Outline each Trypanosoma brucei.
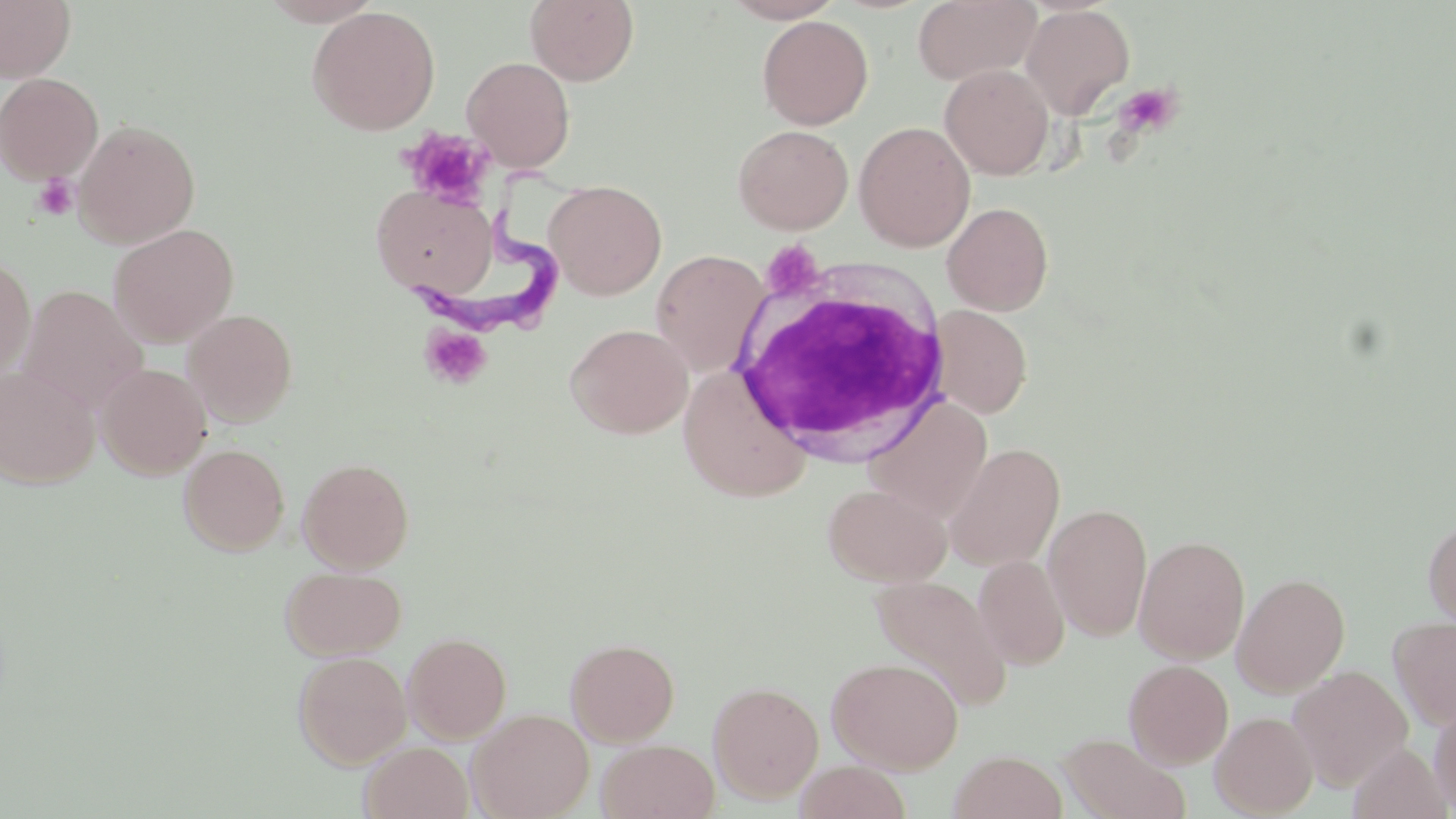
Approximate bounding boxes as (x1, y1, x2, y2) in pixels.
Trypanosoma brucei: (403, 167, 580, 330).

Summary:
  - Platelet locations: (1113, 82, 1183, 139), (401, 129, 494, 209), (32, 173, 80, 221), (760, 240, 825, 302), (419, 323, 492, 390)
  - Uninfected red blood cell locations: (0, 0, 76, 83), (525, 0, 639, 86), (723, 0, 845, 23), (913, 0, 1040, 86), (1020, 4, 1136, 120), (307, 6, 441, 135), (757, 14, 873, 130), (461, 55, 576, 172), (939, 64, 1055, 180), (0, 72, 103, 184), (73, 119, 201, 248), (854, 121, 976, 252), (733, 124, 853, 234), (544, 180, 667, 300), (371, 184, 498, 299), (942, 201, 1054, 316), (108, 224, 239, 347), (650, 249, 771, 376), (0, 256, 36, 381), (18, 285, 148, 414), (928, 305, 1032, 418), (183, 309, 298, 427), (566, 323, 693, 439), (97, 363, 212, 478), (0, 366, 100, 489), (677, 373, 812, 507), (862, 395, 993, 523), (944, 442, 1065, 571), (179, 443, 290, 555), (298, 457, 414, 573), (823, 482, 951, 586), (1043, 503, 1152, 641), (1422, 516, 1456, 629), (1134, 535, 1250, 664), (973, 555, 1070, 670), (280, 565, 406, 660), (1232, 572, 1350, 696), (870, 575, 1012, 711), (1389, 616, 1456, 731), (403, 632, 512, 743), (566, 638, 680, 746), (293, 651, 411, 769), (827, 657, 963, 773), (1124, 659, 1233, 769), (1288, 665, 1413, 791), (708, 680, 824, 804), (1429, 700, 1456, 816), (466, 708, 594, 819), (1210, 711, 1317, 817), (1058, 732, 1192, 819), (597, 739, 720, 819), (360, 741, 474, 819), (1348, 743, 1452, 819), (949, 750, 1067, 819), (794, 760, 913, 819)
  - White blood cell locations: (731, 278, 956, 462)
  - Slide-level diagnosis: Trypanosoma brucei
  - Stain: May-Grünwald-Giemsa
  - Field of view: single
  - Magnification: 1000x
  - Modality: light microscopy
  - Image size: 1456×819 pixels
  - Preparation: thin blood smear